Classify this cell by malaria status.
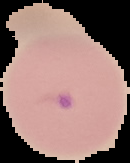
Parasitized.

preparation = thin blood smear
image size = 130×163 pixels
image type = segmented cell region on a black background